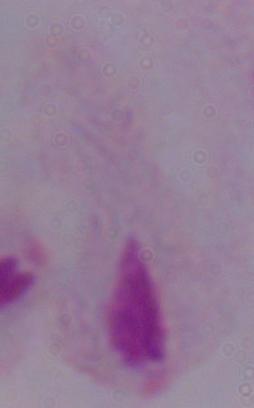

Summary:
  - Modality: photomicrograph
  - Magnification: 1000x
  - Identification: trichomonad